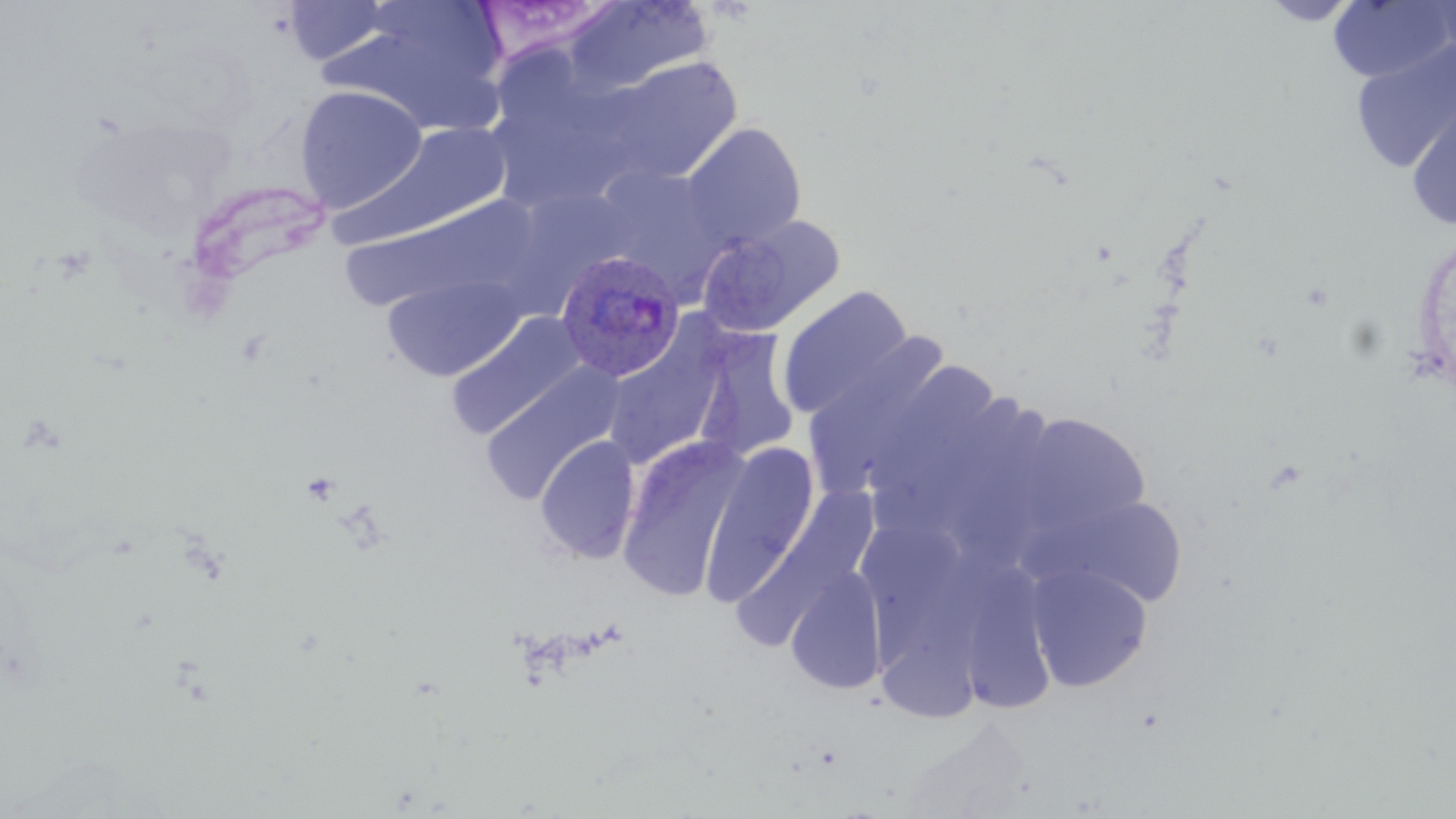

Summary:
  - Coordinate format: approximate bounding boxes as [x1, y1, x2, y2] in pixels
  - Plasmodium ovale-infected red blood cell locations: [555, 249, 686, 382]
  - Uninfected red blood cell locations: [561, 0, 713, 97], [1260, 0, 1362, 25], [281, 1, 396, 65], [1328, 1, 1455, 85], [474, 2, 623, 66], [325, 6, 510, 136], [1351, 39, 1456, 172], [590, 56, 744, 186], [293, 84, 428, 213], [1405, 90, 1456, 231], [336, 122, 514, 249], [681, 122, 806, 250], [337, 196, 537, 314], [696, 215, 845, 336], [382, 273, 527, 381], [777, 286, 913, 421], [445, 311, 588, 441], [602, 323, 730, 469], [692, 327, 800, 464], [808, 336, 946, 497], [863, 360, 999, 506], [479, 362, 624, 506], [1013, 412, 1150, 538], [534, 435, 641, 564], [616, 437, 749, 603], [700, 443, 819, 604], [740, 485, 879, 647], [1057, 494, 1189, 608], [863, 522, 963, 674], [967, 560, 1056, 717], [786, 563, 889, 695], [1026, 563, 1153, 692], [877, 565, 993, 729]
  - Slide-level diagnosis: Plasmodium ovale
  - Field of view: one of a larger specimen
  - Image size: 1456×819 pixels
  - Stain: May-Grünwald-Giemsa
  - Modality: optical microscopy
  - Preparation: thin blood film
  - Magnification: 1000x